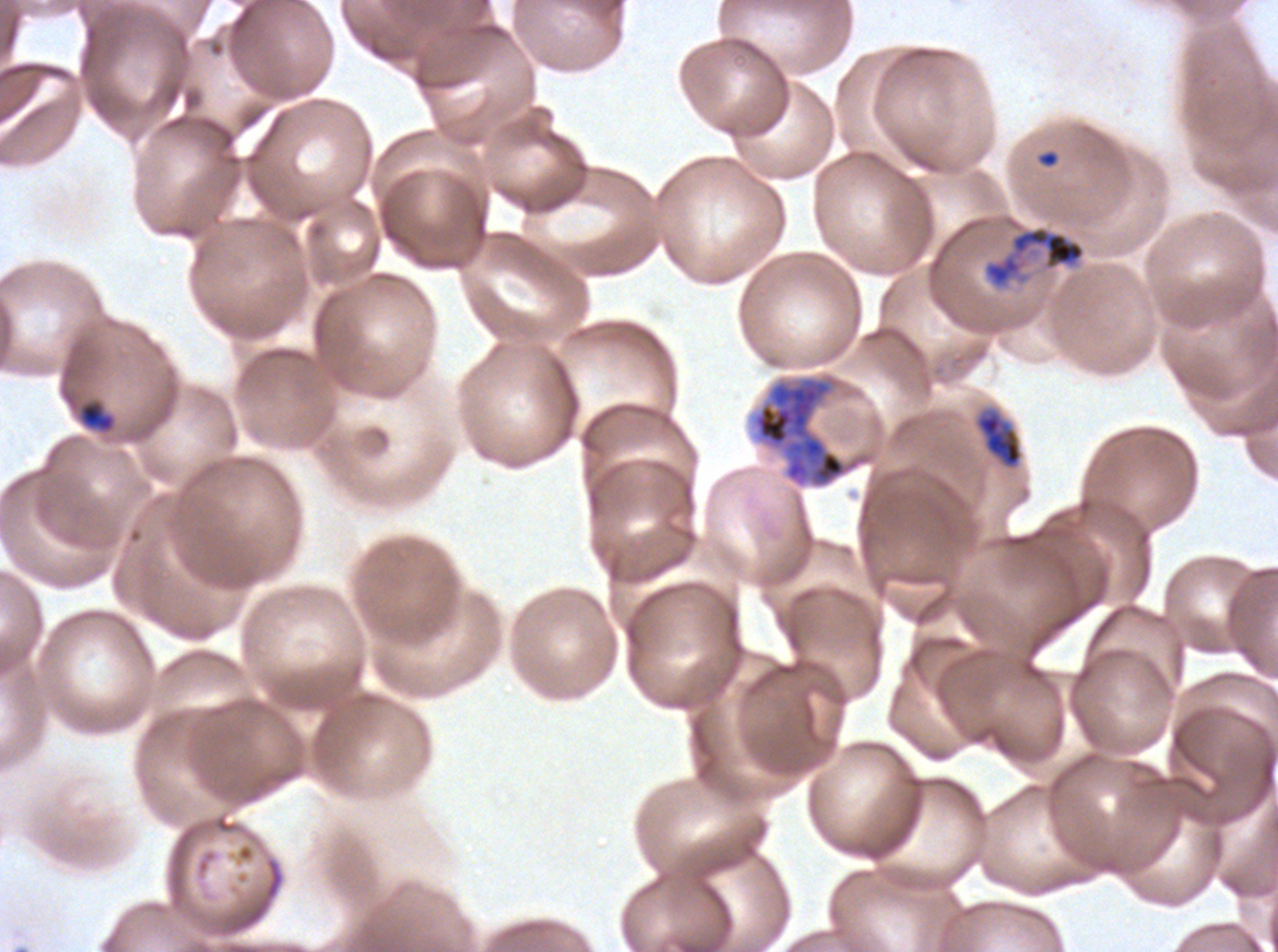
stain: Giemsa
ring_locations: 'approximate bounding boxes as (x1, y1, x2, y2) in pixels: (1037, 149, 1060, 168)'
image_size: 1278×952 pixels
preparation: thin blood film
field_of_view: sub-image separated from a larger composite
early_schizont_locations: 'approximate bounding boxes as (x1, y1, x2, y2) in pixels: (981, 214, 1087, 291), (753, 377, 847, 487)'
life_cycle_stages_observed: ring, late-ring/early-trophozoite, late trophozoite, early schizont
late_trophozoite_locations: 'approximate bounding boxes as (x1, y1, x2, y2) in pixels: (974, 407, 1024, 470)'
specimen: Plasmodium falciparum cultured ex vivo for 24 to 48 hours, from a patient in The Gambia
late_ring_early_trophozoite_locations: 'approximate bounding boxes as (x1, y1, x2, y2) in pixels: (80, 401, 115, 432)'